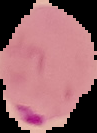
Summary:
  - Preparation: thin blood film
  - Image size: 97×133 pixels
  - Malaria status: parasitized
  - Image type: cell region segmented out of the field of view; surrounding area masked to black